Locate Plasmodium parasites and leukocytes.
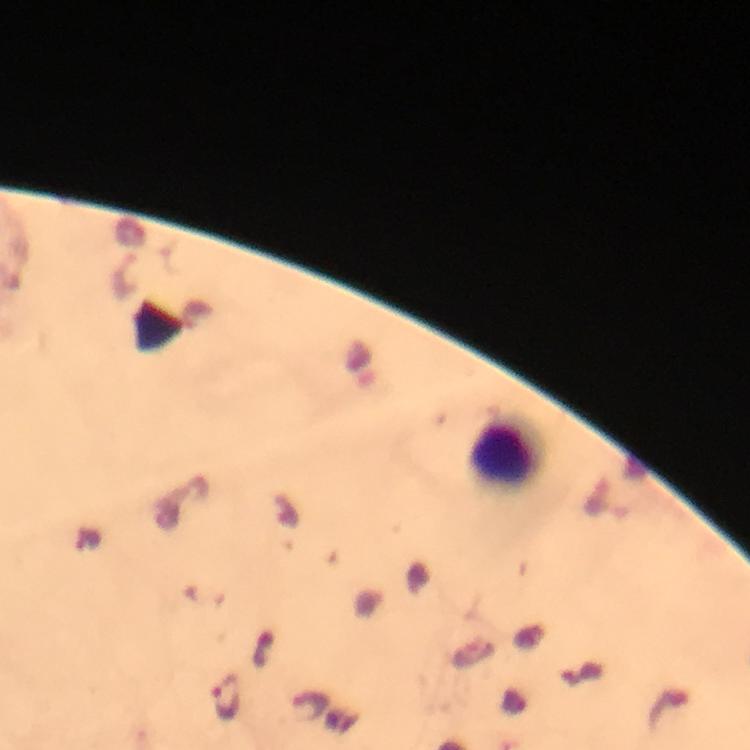
Approximate centers as {x, y} in pixels.
Plasmodium parasites: {364, 364}, {226, 697}, {312, 704}.
Leukocytes: {507, 452}.

stain = Giemsa
preparation = thick blood film
capture = smartphone mounted on the microscope
image size = 750×750 pixels
magnification = 100x
cropped from = a single field of view
context = from a malaria diagnostic workup
immersion oil = used